Identify the cell.
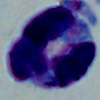

A leukocyte.

Summary:
  - Magnification: 1000x
  - Modality: micrograph